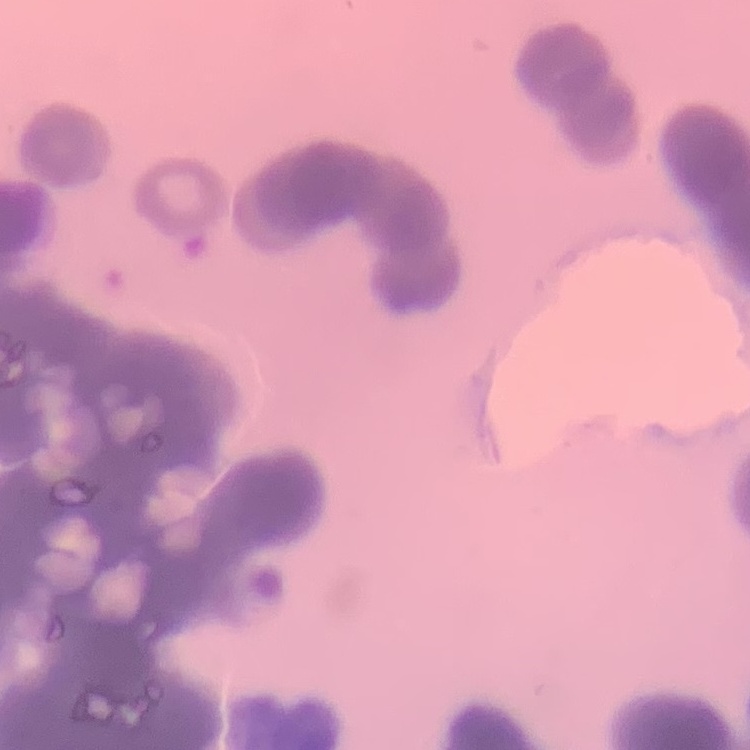

{
  "red_blood_cell_morphology": "rouleaux formation",
  "stain": "Field's or Giemsa",
  "preparation": "thin blood film",
  "image_type": "one tile cut from a larger photomicrograph"
}